Name the parasite shown.
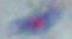
This is Toxoplasma gondii.

magnification = 1000x
modality = micrograph